Locate every Plasmodium falciparum-infected red blood cell.
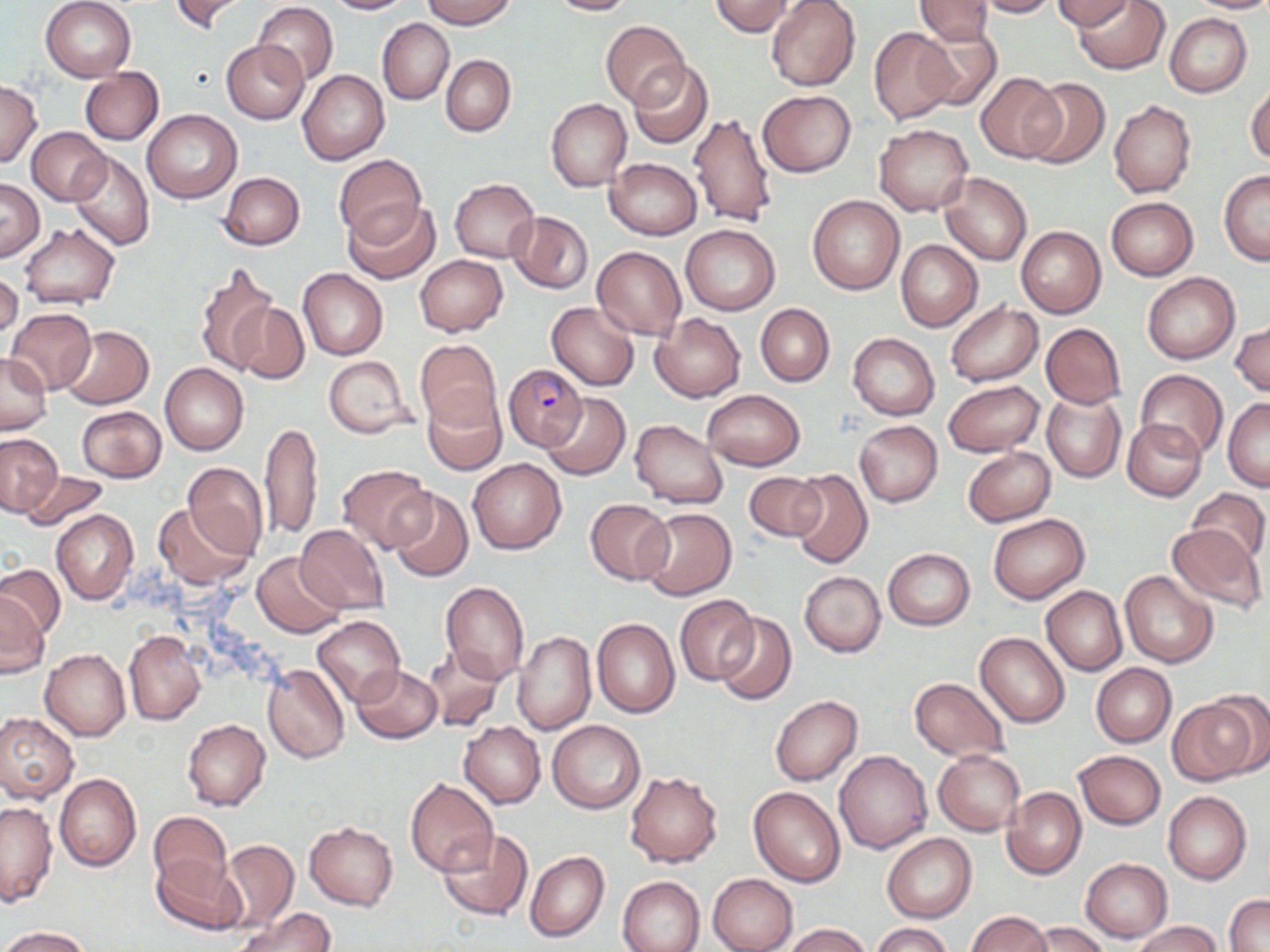

Approximate bounding boxes as [x1, y1, x2, y2] in pixels.
Plasmodium falciparum-infected red blood cells: [503, 363, 586, 452].

{
  "slide_level_diagnosis": "Plasmodium falciparum",
  "stain": "May-Grünwald-Giemsa",
  "uninfected_red_blood_cell_locations": "approximate bounding boxes as [x1, y1, x2, y2] in pixels: [41, 0, 137, 81], [168, 0, 249, 34], [325, 0, 414, 14], [421, 0, 516, 28], [545, 0, 637, 16], [710, 0, 797, 37], [766, 0, 860, 90], [913, 0, 996, 44], [967, 0, 1058, 17], [1072, 0, 1169, 74], [1186, 0, 1270, 13], [1053, 1, 1134, 32], [252, 3, 339, 85], [1165, 13, 1252, 97], [378, 19, 453, 104], [601, 20, 688, 107], [914, 22, 1003, 111], [869, 27, 958, 125], [221, 39, 309, 124], [441, 55, 516, 135], [627, 60, 712, 149], [81, 68, 163, 144], [298, 70, 390, 164], [975, 74, 1062, 163], [1023, 76, 1110, 168], [0, 80, 42, 168], [1247, 83, 1270, 166], [758, 89, 855, 177], [546, 98, 631, 191], [1108, 99, 1196, 197], [142, 109, 242, 203], [689, 112, 777, 228], [875, 124, 973, 216], [27, 126, 108, 204], [68, 151, 155, 251], [335, 153, 426, 245], [605, 157, 702, 239], [1219, 171, 1270, 265], [219, 172, 305, 250], [940, 173, 1032, 265], [0, 178, 44, 260], [450, 179, 540, 262], [807, 195, 904, 294], [1105, 197, 1198, 281], [343, 198, 440, 283], [507, 211, 593, 293], [681, 224, 780, 315], [20, 225, 118, 308], [1016, 226, 1106, 317], [895, 240, 983, 331], [592, 246, 686, 340], [415, 255, 508, 336], [193, 264, 276, 375], [298, 268, 388, 359], [0, 269, 22, 341], [1142, 272, 1240, 363], [227, 301, 309, 386], [547, 301, 639, 390], [944, 302, 1042, 386], [755, 304, 834, 387], [7, 308, 97, 394], [651, 312, 746, 402], [1231, 320, 1269, 397], [1041, 323, 1126, 408], [60, 326, 153, 409], [848, 333, 939, 419], [415, 338, 500, 430], [0, 352, 52, 434], [323, 356, 415, 438], [160, 363, 248, 455], [1135, 370, 1228, 460], [942, 379, 1044, 457], [702, 389, 804, 471], [1041, 389, 1125, 482], [422, 390, 506, 476], [541, 392, 629, 481], [1222, 398, 1270, 491], [76, 406, 167, 482], [1121, 419, 1205, 502], [629, 420, 727, 508], [855, 420, 943, 507], [260, 421, 323, 541], [0, 434, 63, 515], [963, 447, 1055, 526], [467, 458, 567, 554], [182, 463, 268, 558], [338, 464, 432, 552], [787, 468, 872, 569], [18, 469, 109, 530], [742, 471, 827, 542], [388, 488, 473, 582], [1186, 488, 1268, 565], [585, 499, 674, 583], [153, 503, 252, 588], [640, 507, 737, 600], [52, 510, 138, 603], [989, 514, 1089, 604], [1165, 522, 1268, 613], [295, 524, 390, 614], [883, 549, 975, 630], [253, 552, 345, 637], [1, 562, 64, 639], [1120, 570, 1218, 668], [799, 571, 886, 657], [439, 580, 529, 685], [1041, 586, 1127, 675], [0, 592, 50, 679], [674, 595, 760, 686], [714, 613, 797, 705], [312, 615, 405, 703], [591, 618, 680, 717], [124, 630, 206, 725], [513, 632, 596, 735], [975, 632, 1070, 727], [422, 644, 505, 731], [40, 649, 130, 741], [263, 663, 349, 763], [1091, 663, 1176, 746], [350, 664, 442, 743], [909, 677, 1009, 762], [1207, 689, 1270, 778], [770, 695, 863, 786], [1169, 699, 1257, 785], [0, 713, 78, 803], [182, 719, 270, 811], [548, 719, 645, 813], [459, 722, 546, 808], [834, 749, 933, 853], [934, 750, 1025, 835], [1074, 750, 1166, 829], [625, 770, 723, 868], [54, 773, 142, 872], [405, 779, 499, 878], [749, 786, 845, 887], [1002, 786, 1086, 879], [1163, 791, 1252, 884], [0, 801, 57, 906], [147, 811, 232, 892], [305, 821, 399, 911], [437, 828, 533, 920], [882, 834, 976, 922], [220, 840, 298, 931], [525, 850, 609, 942], [153, 854, 247, 936], [1080, 858, 1173, 943], [708, 873, 798, 952], [617, 875, 706, 952], [1225, 894, 1270, 951], [236, 908, 335, 952], [967, 912, 1052, 952], [1027, 921, 1108, 952], [1130, 921, 1224, 952], [870, 922, 954, 952], [782, 923, 870, 952], [0, 927, 90, 951]",
  "magnification": "1000x",
  "modality": "light microscopy",
  "field_of_view": "single",
  "preparation": "thin blood smear",
  "image_size": "1270×952 pixels"
}